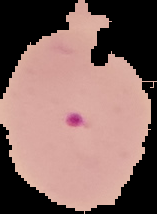

Image is 157×214 pixels. Cell region segmented out of the field of view; the surrounding area is masked to black. Malaria status: parasitized. From a thin blood smear.